Comment on the morphology of the erythrocytes.
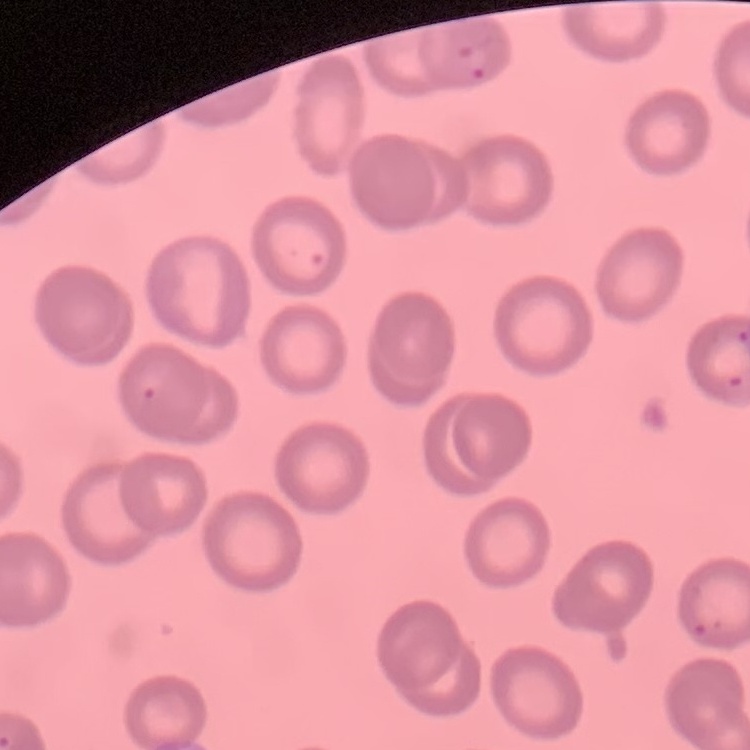

They show no rouleaux formation.

Summary:
  - Preparation: thin blood film
  - Stain: Field's or Giemsa
  - Image type: square crop of a larger photomicrograph